Report the malaria status of this cell.
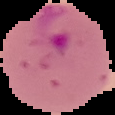
It is parasitized.

preparation = thin blood smear
image size = 115×115 pixels
image type = segmented cell region on a black background